State the preparation type.
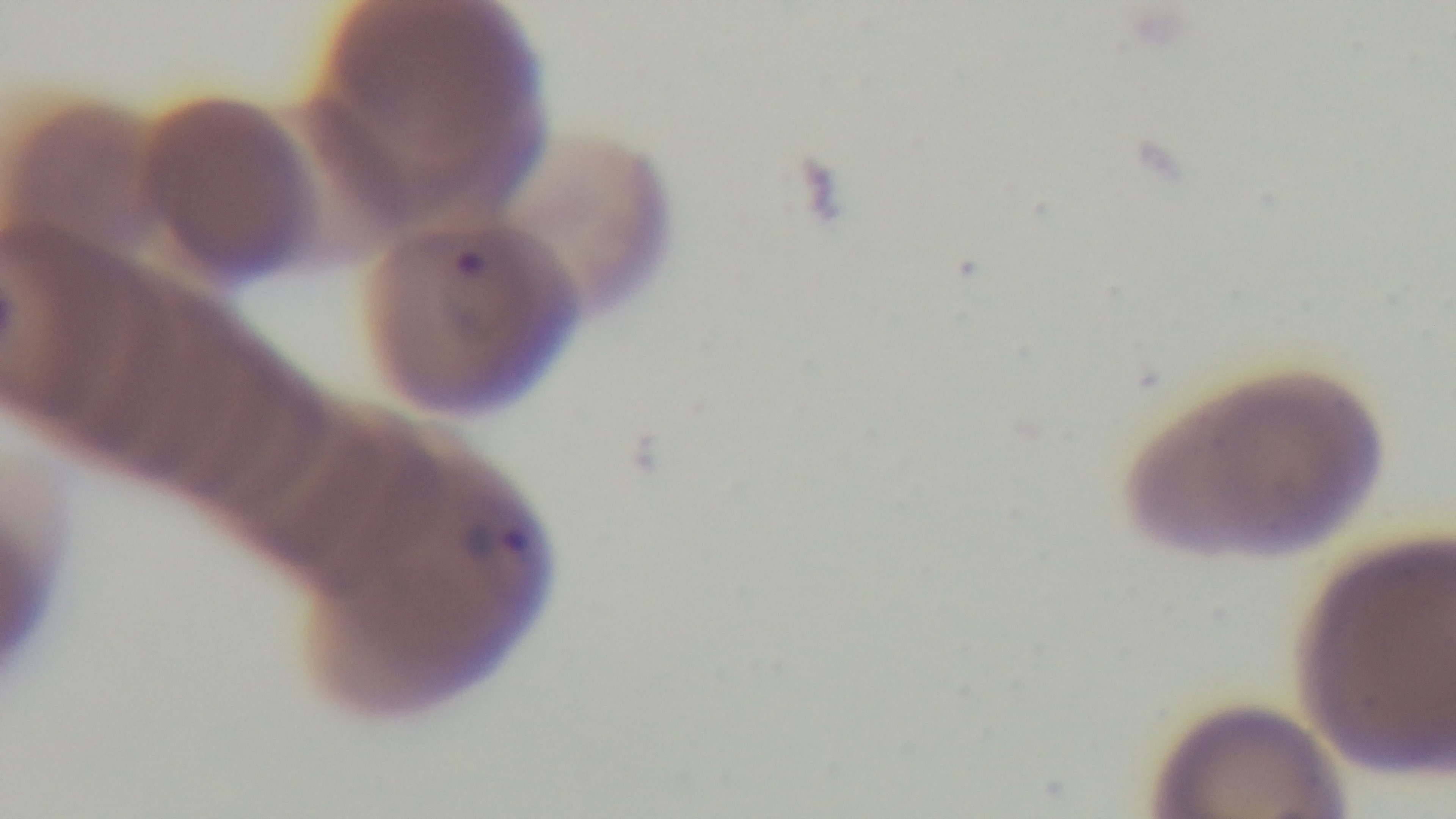

It is a thin blood film.

malaria status = positive
objective = 100x oil immersion
modality = light microscopy
capture = mounted 4K digital camera
field of view = one from the slide
stain = Giemsa